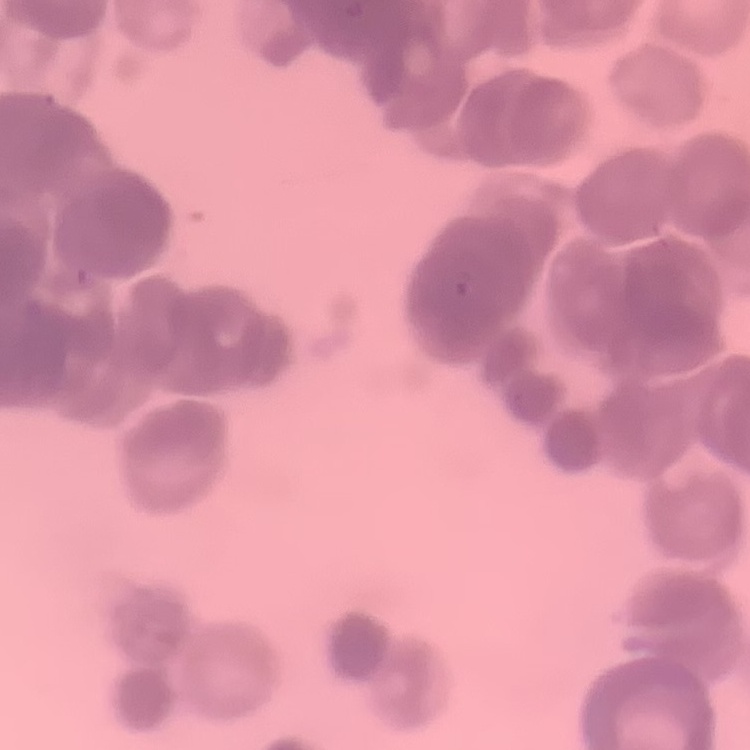
Summary:
  - Red blood cell morphology: rouleaux formation
  - Stain: Field's or Giemsa
  - Image type: square crop of a larger photomicrograph
  - Preparation: thin blood smear